Assess the morphology of the erythrocytes.
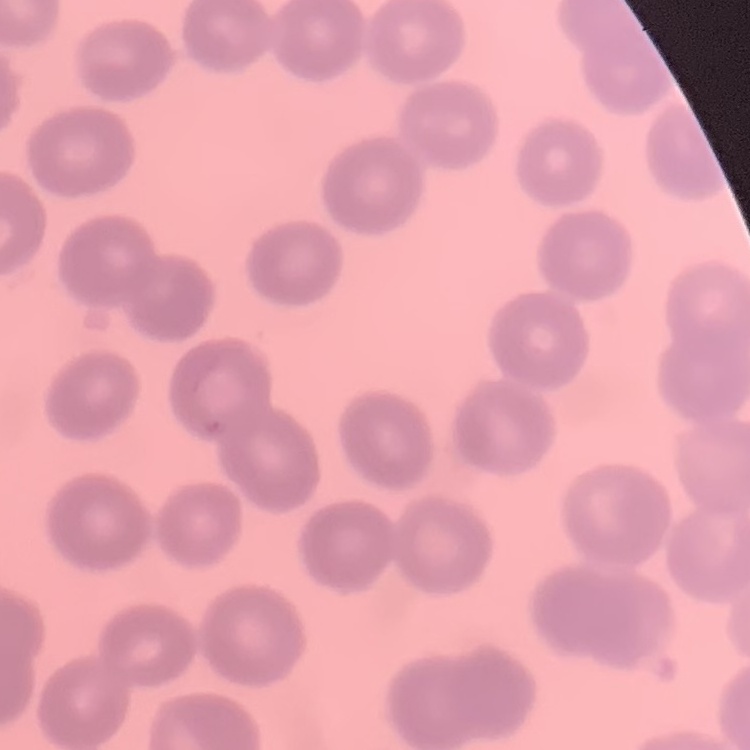
They show no rouleaux formation.

Thin blood smear. Square crop of a larger photomicrograph. Stained with either Field's or Giemsa.